Identify the parasite.
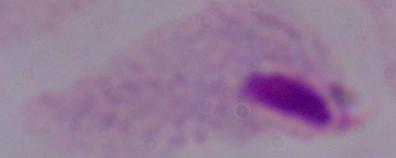

This is a trichomonad.

1000x magnification. Photomicrograph.